Report the malaria status of this cell.
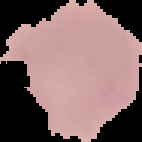

Uninfected.

Summary:
  - Image type: segmented cell region on a black background
  - Preparation: thin blood smear
  - Image size: 142×142 pixels